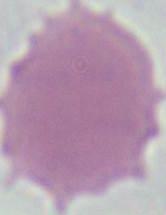
Summary:
  - Magnification: 1000x
  - Modality: photomicrograph
  - Identification: red blood cell